Classify this cell by malaria status.
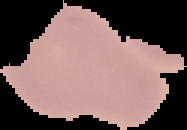

It is uninfected.

The area outside the segmented cell region is set to black. From a thin blood smear. Image is 187×130 pixels.